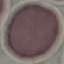

Summary:
  - Malaria status: uninfected
  - Capture: smartphone camera at the microscope eyepiece
  - Preparation: thin blood film
  - Image type: automatically extracted cell patch, resized to 64 × 64 pixels
  - Stain: Giemsa